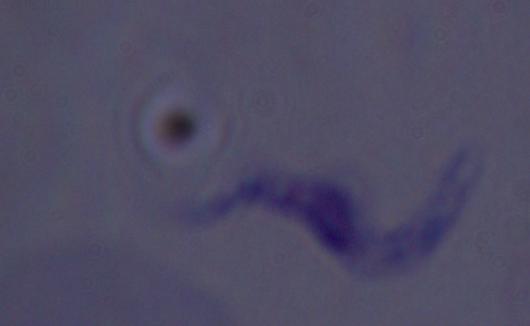

Summary:
  - Magnification: 1000x
  - Identification: trypanosome
  - Modality: photomicrograph